Give the preparation type.
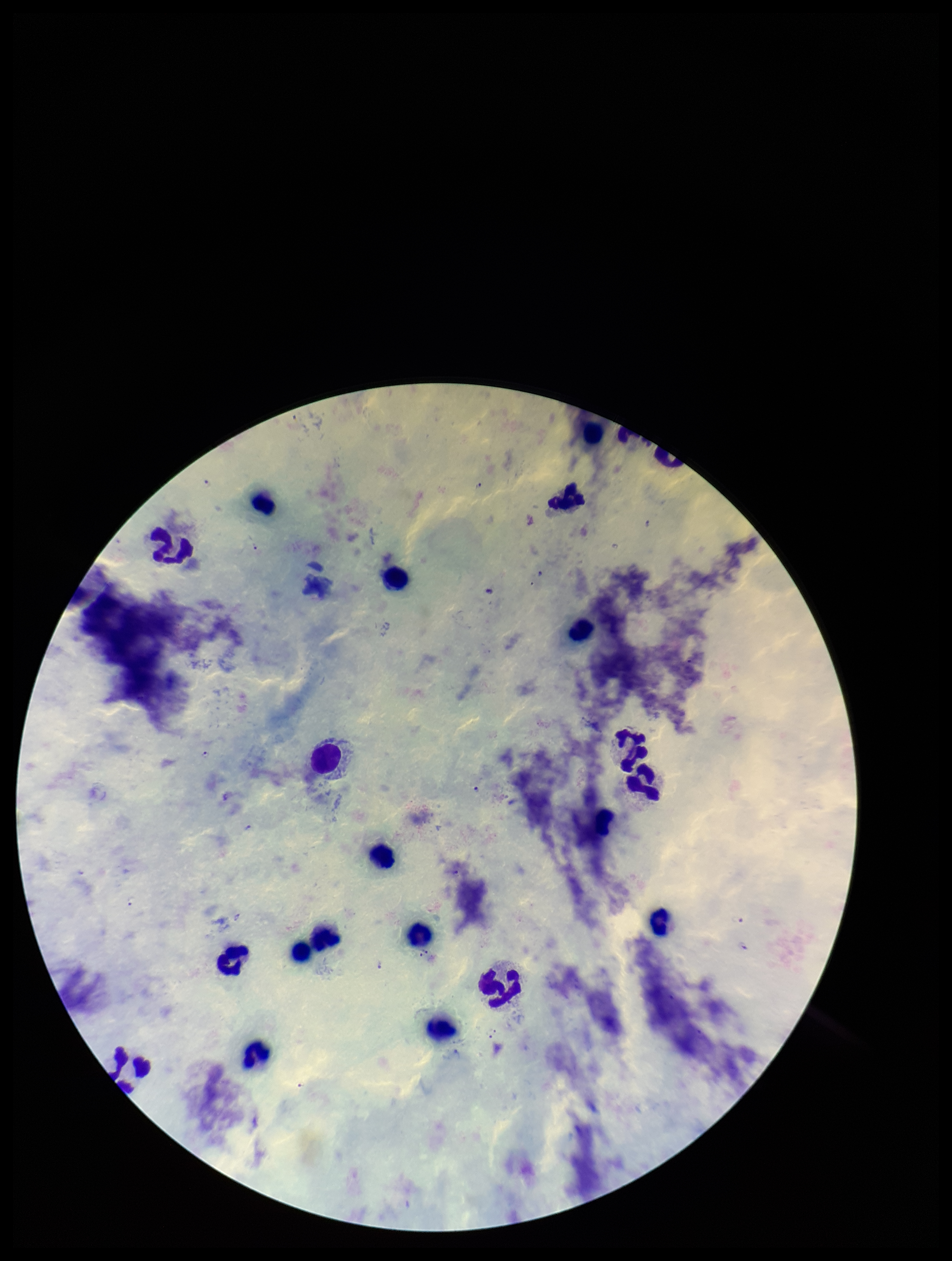
It is a thick blood smear.

Summary:
  - Plasmodium parasites: detected
  - Parasite count: 7
  - Species reported for this patient: Plasmodium falciparum
  - Stain: Giemsa
  - Leukocyte count: 19
  - Patient malaria status: infected
  - Image size: 952×1261 pixels
  - Capture: smartphone photograph through the microscope eyepiece
  - Field of view: single